Locate every uninfected red blood cell.
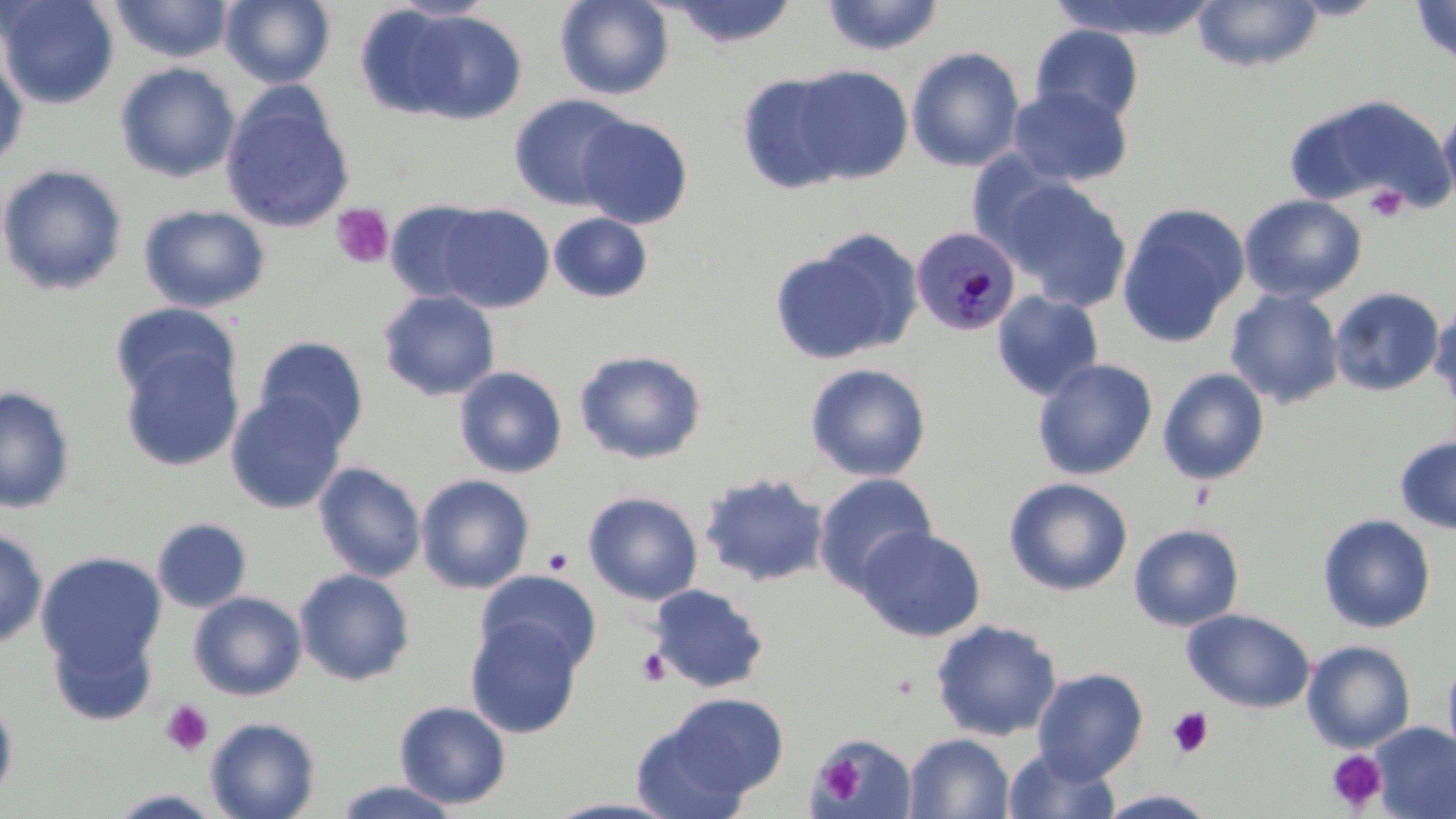
Approximate bounding boxes as [x1, y1, x2, y2] in pixels.
Uninfected red blood cells: [0, 0, 119, 109], [109, 0, 234, 63], [220, 0, 335, 88], [388, 0, 498, 21], [555, 0, 674, 100], [820, 0, 946, 56], [1049, 0, 1219, 41], [1410, 0, 1456, 69], [663, 1, 800, 50], [1192, 1, 1324, 72], [353, 4, 468, 119], [401, 10, 528, 124], [1030, 24, 1145, 126], [906, 46, 1025, 172], [0, 53, 28, 172], [114, 62, 241, 183], [789, 64, 913, 184], [736, 71, 853, 195], [1007, 85, 1132, 187], [219, 87, 355, 235], [508, 93, 635, 210], [1287, 93, 1453, 212], [1438, 100, 1456, 215], [575, 114, 693, 229], [0, 163, 128, 296], [995, 176, 1132, 311], [1239, 194, 1367, 304], [385, 199, 495, 304], [1116, 202, 1250, 349], [138, 204, 270, 313], [436, 204, 554, 312], [548, 213, 653, 303], [769, 231, 920, 365], [1329, 287, 1446, 397], [1225, 288, 1344, 409], [378, 290, 501, 401], [992, 291, 1105, 401], [110, 301, 239, 403], [1430, 303, 1456, 416], [252, 335, 370, 449], [119, 346, 244, 472], [573, 349, 707, 465], [1032, 359, 1158, 480], [805, 363, 931, 481], [454, 366, 568, 479], [1157, 368, 1270, 486], [0, 385, 76, 513], [226, 391, 348, 514], [1394, 434, 1456, 536], [313, 461, 427, 582], [699, 472, 829, 588], [813, 472, 938, 594], [415, 474, 536, 594], [1003, 477, 1133, 596], [583, 491, 704, 606], [1317, 514, 1436, 633], [152, 517, 252, 613], [1129, 524, 1245, 632], [857, 526, 986, 642], [0, 528, 48, 650], [35, 551, 167, 680], [293, 568, 415, 686], [475, 570, 601, 675], [647, 584, 769, 693], [188, 591, 307, 701], [1182, 608, 1315, 713], [465, 616, 584, 738], [930, 619, 1063, 741], [46, 622, 158, 726], [1301, 640, 1416, 753], [1442, 652, 1456, 765], [1032, 667, 1148, 782], [657, 692, 789, 800], [0, 693, 18, 809], [394, 700, 512, 809], [204, 716, 322, 819], [629, 719, 753, 819], [1372, 722, 1456, 818], [811, 733, 917, 818], [904, 733, 1014, 818], [1003, 746, 1121, 819], [331, 780, 463, 818], [105, 789, 226, 818], [1096, 789, 1221, 818], [541, 797, 684, 818].

Platelet locations: [1365, 184, 1409, 222], [330, 203, 394, 268], [543, 547, 573, 574], [635, 647, 671, 686], [160, 700, 214, 756], [1166, 707, 1213, 759], [1326, 750, 1388, 812], [816, 755, 865, 802]. Plasmodium malariae-infected red blood cell locations: [910, 226, 1020, 336]. Slide-level diagnosis: Plasmodium malariae. Single field of view. 1000x magnification. Image is 1456×819 pixels. Thin blood smear. May-Grünwald-Giemsa-stained preparation. Optical microscopy.